Report the malaria status of this cell.
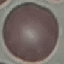

It is uninfected.

Photographed with a smartphone camera at the microscope eyepiece. Thin smear of blood. Giemsa-stained preparation. Automatically extracted cell patch, resized to 64 × 64 pixels.